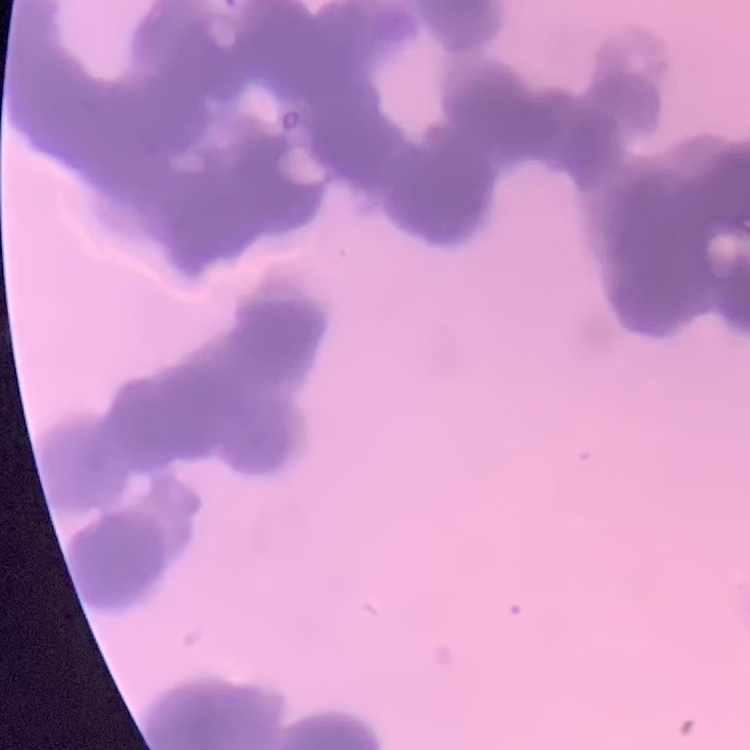 The red blood cells exhibit rouleaux formation. Thin blood smear. Field's or Giemsa stain. Square crop of a larger photomicrograph.